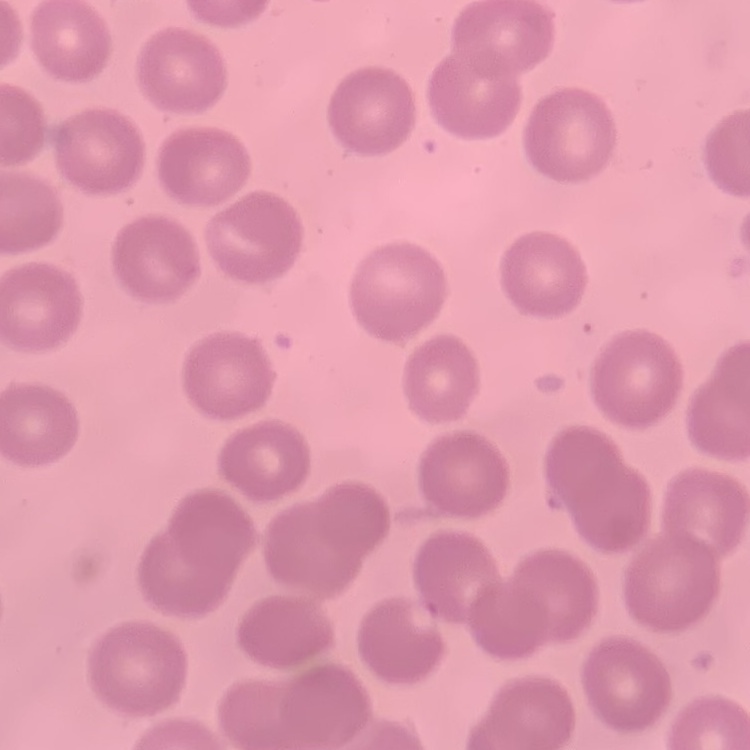

Summary:
  - Erythrocyte morphology: no rouleaux formation
  - Preparation: thin peripheral smear
  - Stain: Field's or Giemsa
  - Image type: one tile cut from a larger photomicrograph